Assess the morphology of the erythrocytes.
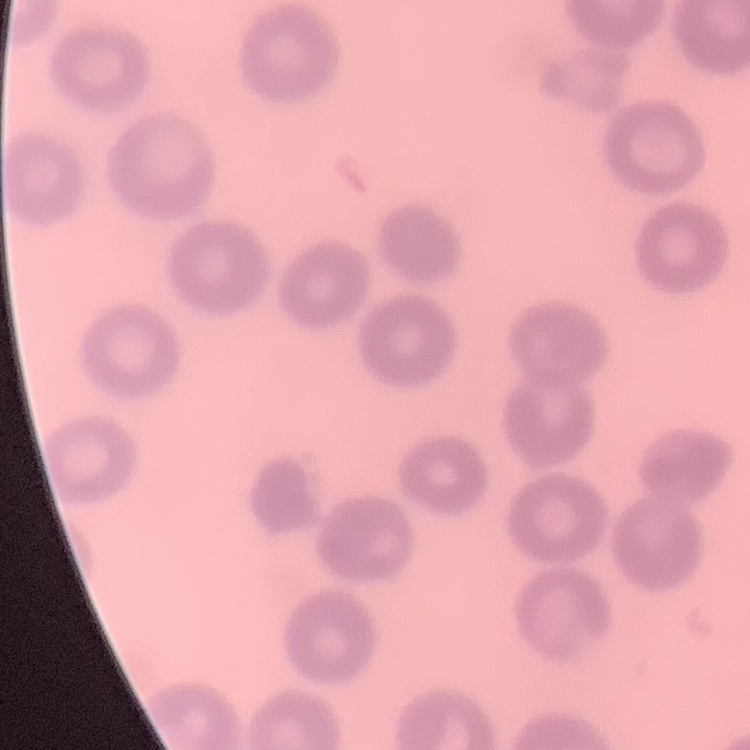

No rouleaux formation.

image type = square crop of a larger photomicrograph
stain = Field's or Giemsa
preparation = thin blood film